Name the cell type shown.
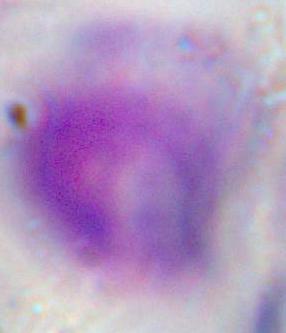
A leukocyte.

magnification = 1000x
modality = micrograph